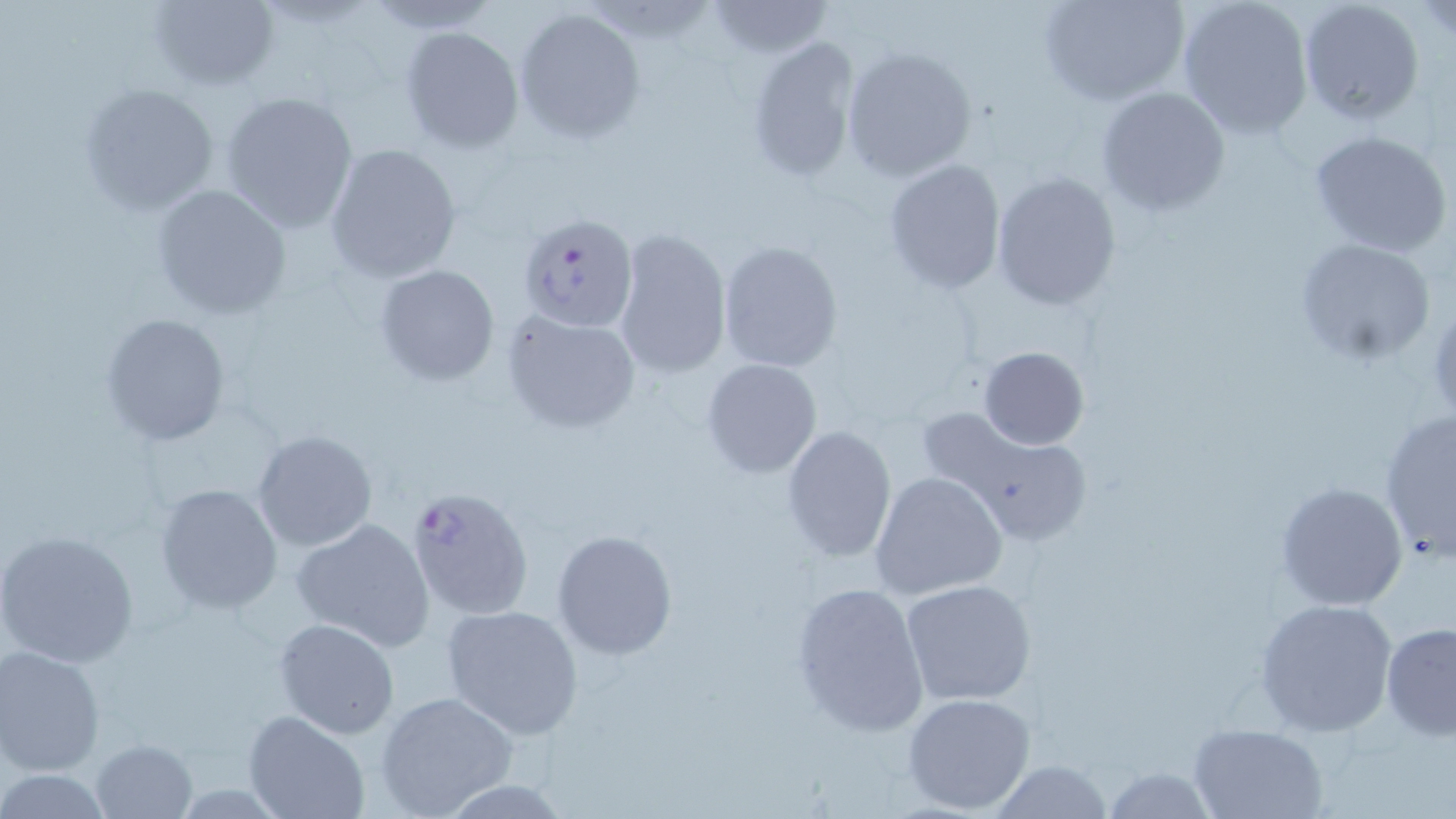

slide_level_diagnosis: Plasmodium falciparum
stain: May-Grünwald-Giemsa
uninfected_red_blood_cell_locations: 'approximate bounding boxes as (x1, y1, x2, y2) in pixels: (148, 0, 279, 91), (1040, 0, 1187, 106), (1177, 0, 1316, 139), (1297, 0, 1426, 126), (704, 1, 836, 59), (1418, 2, 1454, 40), (513, 7, 647, 144), (399, 25, 525, 155), (745, 35, 862, 183), (840, 45, 977, 183), (77, 83, 220, 217), (1095, 86, 1230, 217), (219, 90, 360, 234), (1306, 128, 1452, 257), (323, 143, 462, 283), (882, 160, 1006, 292), (991, 171, 1121, 309), (150, 185, 293, 321), (613, 228, 732, 378), (1294, 236, 1438, 367), (718, 239, 844, 374), (374, 264, 499, 386), (502, 310, 642, 434), (100, 311, 233, 448), (979, 346, 1089, 450), (700, 358, 821, 479), (916, 403, 1091, 545), (1378, 411, 1456, 561), (781, 424, 896, 562), (251, 429, 377, 552), (869, 471, 1007, 600), (1275, 481, 1409, 612), (154, 482, 284, 615), (291, 518, 437, 651), (1, 527, 139, 667), (551, 529, 678, 660), (900, 578, 1037, 707), (790, 584, 928, 734), (1254, 597, 1399, 737), (440, 603, 588, 741), (275, 618, 399, 738), (1379, 621, 1456, 739), (0, 646, 106, 777), (375, 690, 518, 817), (902, 692, 1036, 815), (244, 711, 367, 819), (1189, 722, 1330, 819), (90, 739, 198, 819), (987, 760, 1118, 817), (1098, 765, 1218, 818), (0, 769, 115, 816)'
preparation: thin blood smear
modality: optical microscopy
magnification: 1000x
plasmodium_falciparum_infected_red_blood_cell_locations: 'approximate bounding boxes as (x1, y1, x2, y2) in pixels: (517, 214, 637, 332), (405, 482, 533, 619)'
image_size: 1456×819 pixels
field_of_view: one of a larger specimen